Identify the parasite.
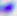
Toxoplasma gondii.

Captured at 400x magnification. Micrograph.